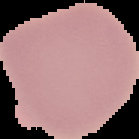
Segmented cell region on a black background. Result: negative for Plasmodium parasites. From a thin blood film. Image is 139×139 pixels.